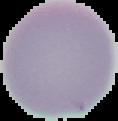
Summary:
  - Result: negative for malaria parasites
  - Image size: 118×121 pixels
  - Image type: segmented cell region on a black background
  - Preparation: thin blood smear